State the blood parasite species.
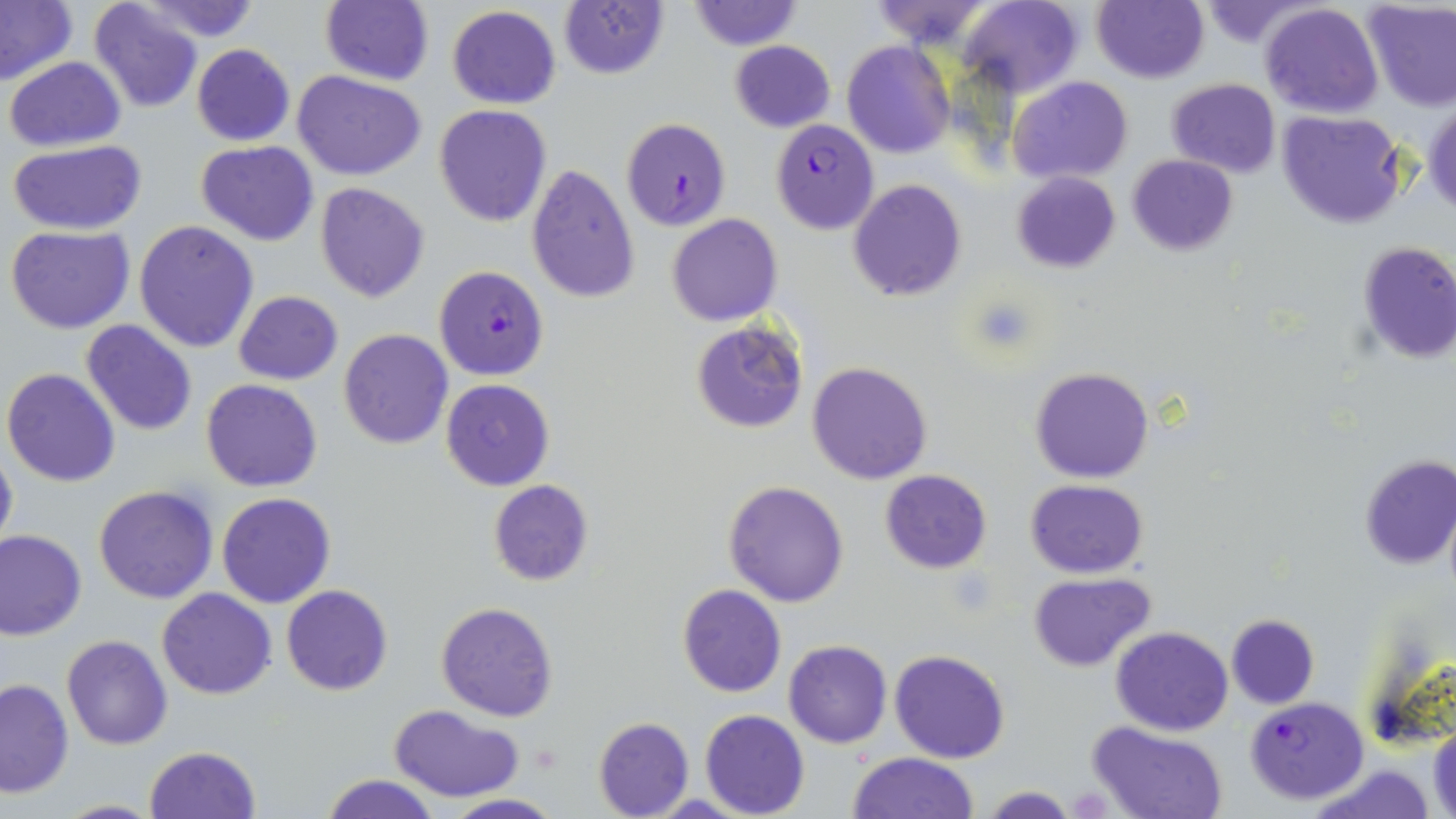
Plasmodium falciparum.

Summary:
  - Coordinate format: approximate bounding boxes as [x1, y1, x2, y2] in pixels
  - Plasmodium falciparum-infected red blood cell locations: [621, 118, 730, 231], [770, 119, 879, 234], [434, 265, 549, 381], [1244, 695, 1369, 805]
  - Uninfected red blood cell locations: [0, 0, 78, 88], [88, 0, 203, 114], [132, 0, 265, 42], [684, 0, 803, 50], [865, 0, 997, 48], [958, 0, 1083, 98], [1092, 0, 1209, 83], [318, 1, 435, 86], [1190, 1, 1323, 46], [1362, 1, 1456, 111], [1260, 2, 1383, 117], [559, 3, 669, 79], [446, 6, 562, 110], [729, 39, 835, 132], [842, 40, 955, 158], [190, 44, 294, 146], [5, 56, 126, 151], [293, 69, 427, 181], [1008, 76, 1131, 185], [1164, 78, 1282, 178], [1425, 102, 1456, 216], [433, 104, 553, 227], [1278, 110, 1407, 229], [7, 139, 149, 236], [196, 140, 320, 247], [1126, 154, 1238, 256], [525, 163, 639, 304], [1011, 171, 1121, 273], [848, 179, 966, 301], [314, 182, 430, 302], [667, 213, 782, 326], [134, 221, 258, 354], [5, 225, 135, 333], [1355, 240, 1456, 365], [234, 290, 343, 384], [690, 318, 808, 432], [81, 320, 196, 436], [338, 328, 453, 449], [17, 331, 175, 459], [806, 361, 932, 484], [1029, 367, 1155, 483], [3, 368, 121, 487], [201, 378, 323, 492], [441, 378, 554, 492], [0, 441, 17, 562], [1357, 455, 1456, 571], [881, 469, 991, 573], [724, 479, 851, 607], [1024, 479, 1149, 579], [487, 481, 595, 587], [93, 485, 218, 603], [216, 493, 338, 608], [0, 530, 86, 640], [1028, 573, 1156, 672], [280, 585, 393, 696], [677, 585, 786, 697], [155, 587, 277, 698], [436, 601, 557, 721], [1226, 613, 1319, 709], [1111, 626, 1233, 735], [62, 634, 172, 750], [784, 641, 892, 748], [889, 649, 1011, 763], [0, 678, 73, 798], [390, 704, 524, 803], [699, 709, 810, 819], [593, 717, 693, 818], [1087, 720, 1229, 819], [1429, 723, 1456, 818], [143, 746, 261, 819], [846, 751, 981, 818], [1304, 762, 1438, 819], [321, 774, 440, 819], [981, 786, 1075, 818], [441, 793, 564, 818], [47, 799, 167, 818]
  - Platelet locations: [531, 744, 564, 771]
  - Preparation: thin blood film
  - Stain: May-Grünwald-Giemsa
  - Magnification: 1000x
  - Image size: 1456×819 pixels
  - Field of view: one of a larger specimen
  - Modality: light microscopy